Give the extent of all Plasmodium malariae-infected red blood cells.
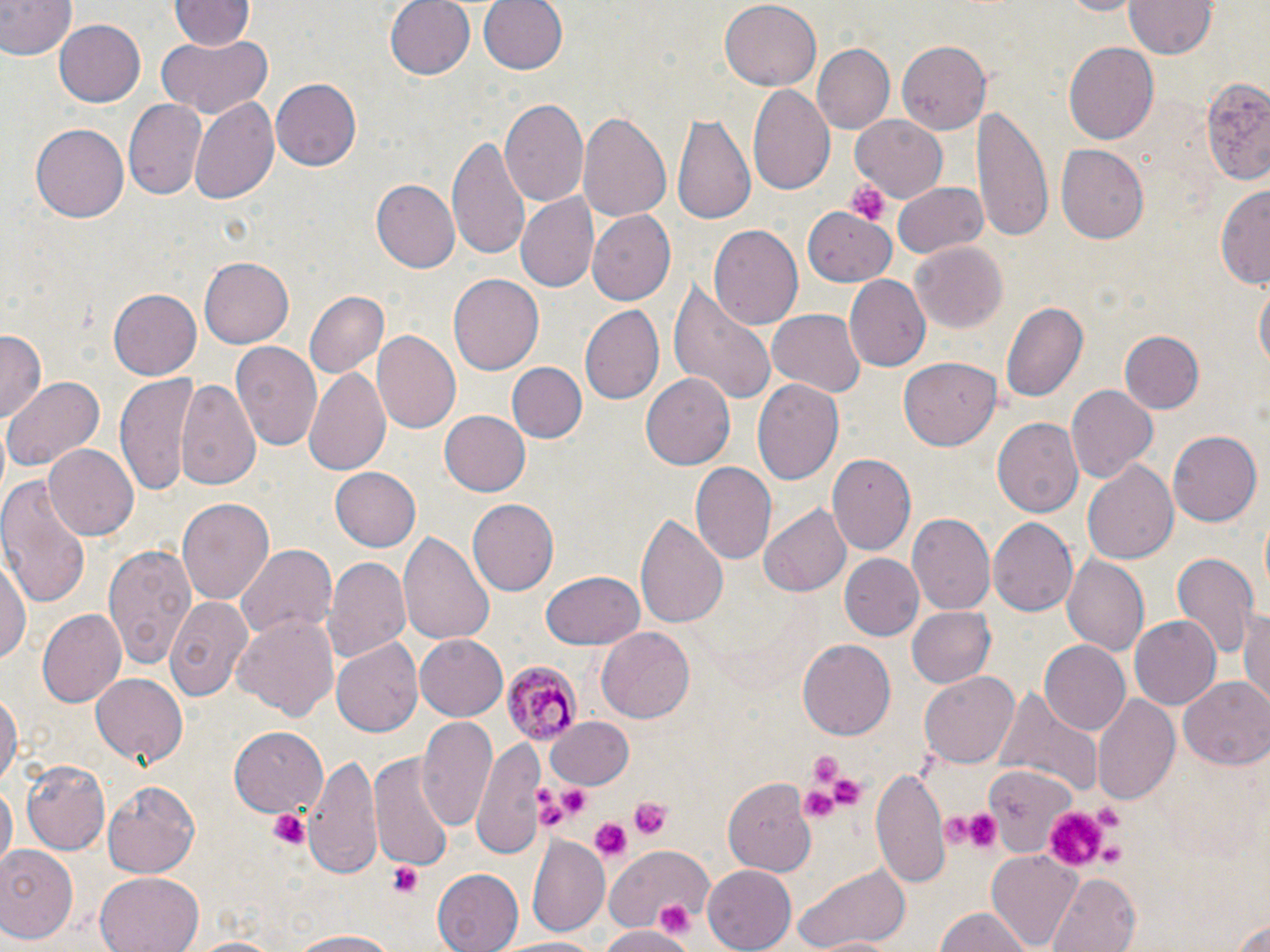
Approximate bounding boxes as named x1/y1/x2/y2 corners in pixels.
Plasmodium malariae-infected red blood cells: (x1=503, y1=658, x2=583, y2=745).

{
  "slide_level_diagnosis": "Plasmodium malariae",
  "magnification": "1000x",
  "field_of_view": "one of a larger specimen",
  "image_size": "1270×952 pixels",
  "preparation": "thin blood film",
  "modality": "light microscopy",
  "uninfected_red_blood_cell_locations": "approximate bounding boxes as named x1/y1/x2/y2 corners in pixels: (x1=384, y1=0, x2=476, y2=81), (x1=477, y1=0, x2=568, y2=78), (x1=720, y1=0, x2=820, y2=88), (x1=1051, y1=0, x2=1147, y2=17), (x1=1123, y1=0, x2=1220, y2=58), (x1=0, y1=1, x2=73, y2=60), (x1=171, y1=1, x2=254, y2=52), (x1=162, y1=5, x2=262, y2=91), (x1=54, y1=19, x2=146, y2=107), (x1=154, y1=34, x2=273, y2=118), (x1=896, y1=42, x2=991, y2=135), (x1=1061, y1=42, x2=1159, y2=145), (x1=813, y1=44, x2=895, y2=133), (x1=1199, y1=75, x2=1270, y2=187), (x1=270, y1=79, x2=362, y2=171), (x1=747, y1=83, x2=835, y2=198), (x1=189, y1=97, x2=279, y2=208), (x1=121, y1=98, x2=209, y2=203), (x1=501, y1=99, x2=589, y2=209), (x1=973, y1=106, x2=1051, y2=238), (x1=577, y1=109, x2=674, y2=226), (x1=673, y1=111, x2=754, y2=229), (x1=852, y1=116, x2=948, y2=203), (x1=31, y1=124, x2=128, y2=221), (x1=448, y1=133, x2=534, y2=264), (x1=1057, y1=145, x2=1149, y2=243), (x1=891, y1=180, x2=989, y2=259), (x1=373, y1=181, x2=457, y2=272), (x1=1217, y1=184, x2=1270, y2=287), (x1=517, y1=194, x2=600, y2=294), (x1=586, y1=211, x2=676, y2=305), (x1=808, y1=211, x2=894, y2=285), (x1=708, y1=225, x2=803, y2=332), (x1=911, y1=242, x2=1009, y2=332), (x1=197, y1=256, x2=293, y2=348), (x1=450, y1=275, x2=544, y2=373), (x1=844, y1=275, x2=931, y2=372), (x1=669, y1=280, x2=779, y2=405), (x1=1253, y1=281, x2=1269, y2=380), (x1=109, y1=289, x2=201, y2=378), (x1=307, y1=292, x2=387, y2=378), (x1=1001, y1=300, x2=1089, y2=405), (x1=581, y1=305, x2=664, y2=404), (x1=769, y1=310, x2=865, y2=397), (x1=0, y1=331, x2=44, y2=423), (x1=372, y1=331, x2=461, y2=432), (x1=1121, y1=331, x2=1204, y2=415), (x1=231, y1=341, x2=323, y2=453), (x1=899, y1=358, x2=1001, y2=451), (x1=506, y1=361, x2=587, y2=444), (x1=302, y1=367, x2=393, y2=477), (x1=116, y1=373, x2=197, y2=496), (x1=641, y1=373, x2=736, y2=471), (x1=5, y1=376, x2=102, y2=472), (x1=176, y1=378, x2=260, y2=492), (x1=753, y1=378, x2=844, y2=485), (x1=1066, y1=385, x2=1156, y2=481), (x1=437, y1=409, x2=531, y2=496), (x1=993, y1=418, x2=1083, y2=520), (x1=1168, y1=431, x2=1261, y2=527), (x1=44, y1=444, x2=139, y2=542), (x1=828, y1=453, x2=916, y2=555), (x1=1084, y1=461, x2=1179, y2=563), (x1=692, y1=464, x2=777, y2=565), (x1=331, y1=467, x2=421, y2=551), (x1=0, y1=476, x2=90, y2=609), (x1=177, y1=495, x2=275, y2=608), (x1=467, y1=498, x2=559, y2=596), (x1=757, y1=506, x2=850, y2=597), (x1=636, y1=513, x2=727, y2=630), (x1=909, y1=514, x2=996, y2=615), (x1=988, y1=517, x2=1077, y2=618), (x1=397, y1=530, x2=495, y2=647), (x1=100, y1=538, x2=198, y2=671), (x1=236, y1=543, x2=336, y2=647), (x1=1, y1=550, x2=31, y2=674), (x1=1169, y1=550, x2=1259, y2=660), (x1=839, y1=554, x2=925, y2=642), (x1=1060, y1=554, x2=1149, y2=655), (x1=326, y1=556, x2=412, y2=665), (x1=541, y1=571, x2=645, y2=649), (x1=165, y1=596, x2=253, y2=701), (x1=905, y1=605, x2=995, y2=687), (x1=38, y1=606, x2=125, y2=709), (x1=1240, y1=606, x2=1269, y2=707), (x1=1130, y1=615, x2=1223, y2=710), (x1=232, y1=616, x2=337, y2=719), (x1=596, y1=627, x2=694, y2=724), (x1=416, y1=634, x2=508, y2=721), (x1=332, y1=638, x2=421, y2=737), (x1=798, y1=638, x2=897, y2=740), (x1=1039, y1=641, x2=1131, y2=736), (x1=919, y1=669, x2=1019, y2=767), (x1=90, y1=673, x2=187, y2=765), (x1=1181, y1=677, x2=1270, y2=771), (x1=998, y1=686, x2=1102, y2=799), (x1=0, y1=687, x2=20, y2=794), (x1=1092, y1=693, x2=1180, y2=805), (x1=546, y1=715, x2=635, y2=790), (x1=417, y1=716, x2=499, y2=834), (x1=230, y1=726, x2=328, y2=816), (x1=472, y1=736, x2=548, y2=861), (x1=302, y1=750, x2=384, y2=880), (x1=371, y1=757, x2=453, y2=870), (x1=21, y1=759, x2=111, y2=854), (x1=982, y1=764, x2=1072, y2=853), (x1=872, y1=766, x2=947, y2=886), (x1=103, y1=778, x2=201, y2=878), (x1=726, y1=778, x2=816, y2=876), (x1=0, y1=781, x2=15, y2=872), (x1=526, y1=833, x2=609, y2=936), (x1=607, y1=843, x2=714, y2=940), (x1=0, y1=846, x2=80, y2=944), (x1=987, y1=851, x2=1084, y2=950), (x1=793, y1=861, x2=911, y2=950), (x1=704, y1=864, x2=798, y2=951), (x1=433, y1=866, x2=528, y2=952), (x1=94, y1=871, x2=203, y2=952), (x1=1049, y1=873, x2=1141, y2=952), (x1=932, y1=907, x2=1040, y2=952), (x1=1227, y1=910, x2=1270, y2=951), (x1=598, y1=926, x2=693, y2=952), (x1=281, y1=929, x2=408, y2=950), (x1=500, y1=934, x2=606, y2=952), (x1=178, y1=935, x2=289, y2=952)",
  "stain": "May-Grünwald-Giemsa",
  "platelet_locations": "approximate bounding boxes as named x1/y1/x2/y2 corners in pixels: (x1=846, y1=180, x2=888, y2=227), (x1=803, y1=751, x2=848, y2=791), (x1=829, y1=777, x2=861, y2=809), (x1=556, y1=780, x2=594, y2=819), (x1=529, y1=783, x2=557, y2=805), (x1=796, y1=785, x2=840, y2=825), (x1=630, y1=797, x2=673, y2=841), (x1=1089, y1=801, x2=1124, y2=830), (x1=533, y1=803, x2=572, y2=831), (x1=268, y1=806, x2=312, y2=850), (x1=1045, y1=806, x2=1114, y2=870), (x1=941, y1=811, x2=971, y2=848), (x1=964, y1=812, x2=1003, y2=849), (x1=589, y1=818, x2=630, y2=860), (x1=1100, y1=839, x2=1127, y2=866), (x1=389, y1=861, x2=424, y2=899), (x1=653, y1=900, x2=696, y2=938)"
}